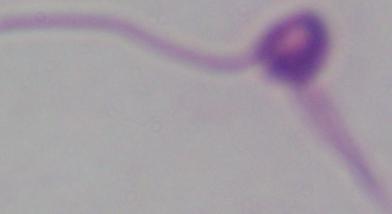 Photomicrograph. 1000x magnification. A Leishmania parasite is shown.